Describe the morphology of the erythrocytes.
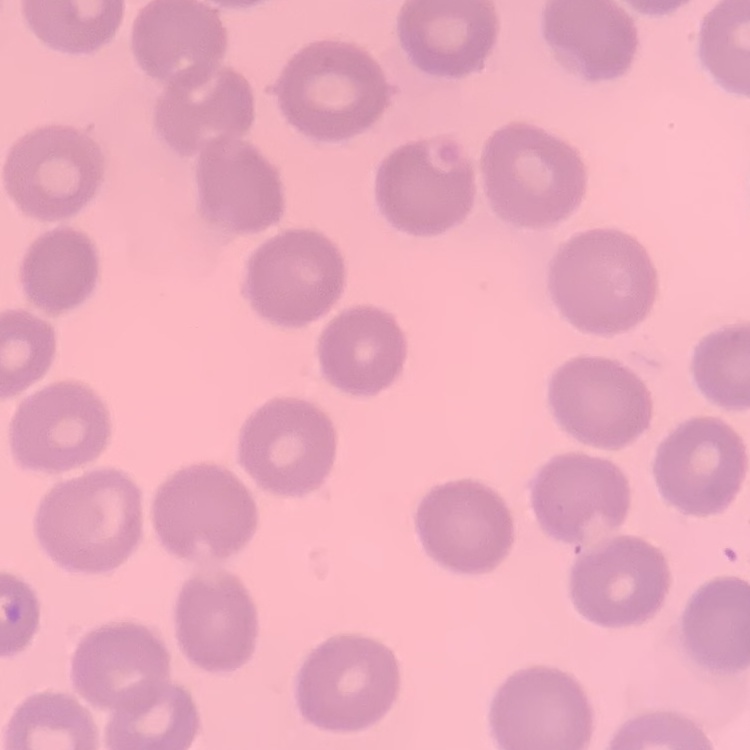

They show no rouleaux formation.

Thin peripheral smear. One tile cut from a larger photomicrograph. Stained with either Field's or Giemsa.